Locate every blood parasite and identify its species.
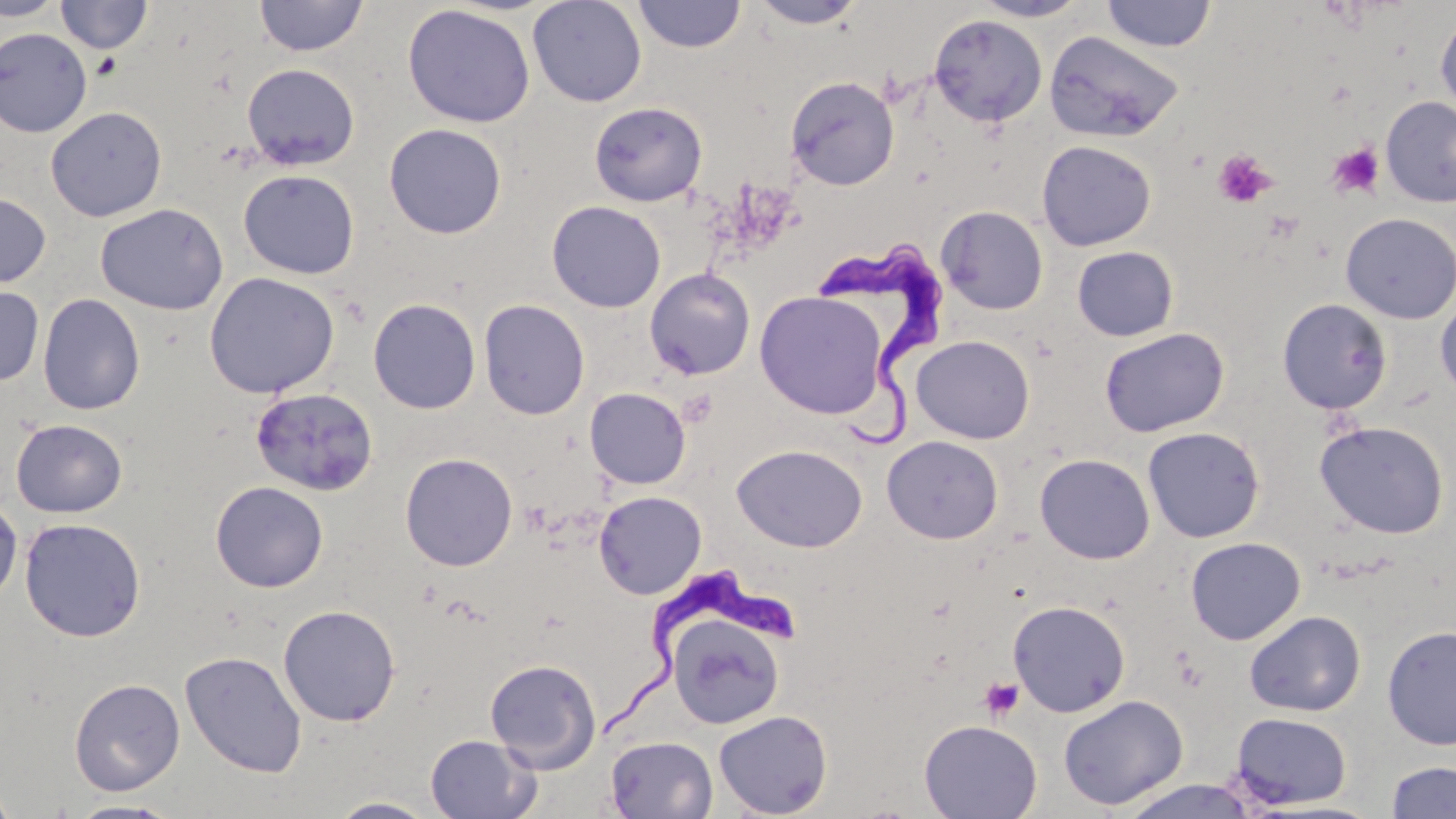

Approximate bounding boxes as named x1/y1/x2/y2 corners in pixels.
Trypanosoma brucei: (x1=819, y1=240, x2=949, y2=448), (x1=607, y1=565, x2=807, y2=738).
No Plasmodium falciparum, Plasmodium ovale, Plasmodium malariae, Plasmodium vivax, or Babesia divergens observed.

Summary:
  - Uninfected red blood cell locations: (x1=0, y1=0, x2=66, y2=21), (x1=56, y1=0, x2=152, y2=54), (x1=254, y1=0, x2=368, y2=57), (x1=528, y1=0, x2=647, y2=108), (x1=632, y1=0, x2=747, y2=53), (x1=971, y1=0, x2=1091, y2=22), (x1=1101, y1=0, x2=1217, y2=52), (x1=747, y1=1, x2=868, y2=29), (x1=402, y1=4, x2=536, y2=128), (x1=1435, y1=11, x2=1456, y2=117), (x1=928, y1=14, x2=1047, y2=127), (x1=0, y1=28, x2=92, y2=137), (x1=1043, y1=30, x2=1186, y2=143), (x1=242, y1=63, x2=360, y2=170), (x1=785, y1=76, x2=899, y2=190), (x1=1380, y1=96, x2=1456, y2=207), (x1=589, y1=102, x2=707, y2=207), (x1=45, y1=106, x2=167, y2=222), (x1=383, y1=123, x2=507, y2=239), (x1=1036, y1=140, x2=1156, y2=251), (x1=238, y1=169, x2=360, y2=280), (x1=0, y1=193, x2=51, y2=288), (x1=546, y1=200, x2=666, y2=313), (x1=95, y1=203, x2=229, y2=315), (x1=936, y1=206, x2=1048, y2=314), (x1=1340, y1=213, x2=1456, y2=323), (x1=1072, y1=246, x2=1179, y2=341), (x1=644, y1=268, x2=756, y2=380), (x1=204, y1=272, x2=340, y2=398), (x1=0, y1=284, x2=44, y2=386), (x1=755, y1=291, x2=889, y2=418), (x1=37, y1=293, x2=145, y2=415), (x1=1435, y1=295, x2=1456, y2=400), (x1=368, y1=298, x2=481, y2=414), (x1=1277, y1=298, x2=1393, y2=415), (x1=478, y1=299, x2=590, y2=420), (x1=1099, y1=327, x2=1229, y2=438), (x1=911, y1=335, x2=1035, y2=443), (x1=250, y1=386, x2=379, y2=496), (x1=585, y1=387, x2=691, y2=489), (x1=11, y1=418, x2=127, y2=518), (x1=1314, y1=420, x2=1450, y2=539), (x1=1142, y1=426, x2=1265, y2=542), (x1=882, y1=435, x2=1003, y2=544), (x1=731, y1=443, x2=868, y2=552), (x1=400, y1=452, x2=518, y2=571), (x1=1034, y1=453, x2=1155, y2=564), (x1=210, y1=481, x2=328, y2=593), (x1=593, y1=491, x2=706, y2=599), (x1=0, y1=495, x2=23, y2=605), (x1=19, y1=517, x2=146, y2=642), (x1=1185, y1=536, x2=1306, y2=645), (x1=1007, y1=600, x2=1131, y2=717), (x1=278, y1=604, x2=401, y2=726), (x1=1244, y1=610, x2=1366, y2=716), (x1=668, y1=615, x2=784, y2=729), (x1=1382, y1=625, x2=1456, y2=750), (x1=180, y1=650, x2=307, y2=778), (x1=485, y1=658, x2=601, y2=773), (x1=69, y1=678, x2=185, y2=796), (x1=1058, y1=694, x2=1189, y2=811), (x1=713, y1=710, x2=833, y2=818), (x1=1229, y1=712, x2=1353, y2=809), (x1=918, y1=719, x2=1042, y2=819), (x1=425, y1=734, x2=541, y2=819), (x1=605, y1=735, x2=718, y2=818), (x1=1385, y1=761, x2=1456, y2=818), (x1=1116, y1=779, x2=1262, y2=819), (x1=0, y1=782, x2=18, y2=819), (x1=325, y1=797, x2=442, y2=818), (x1=65, y1=799, x2=184, y2=818)
  - Platelet locations: (x1=1326, y1=142, x2=1386, y2=200), (x1=1212, y1=148, x2=1277, y2=208), (x1=979, y1=676, x2=1024, y2=721)
  - Slide-level diagnosis: Trypanosoma brucei
  - Preparation: thin blood film
  - Field of view: single
  - Magnification: 1000x
  - Modality: light microscopy
  - Image size: 1456×819 pixels
  - Stain: May-Grünwald-Giemsa